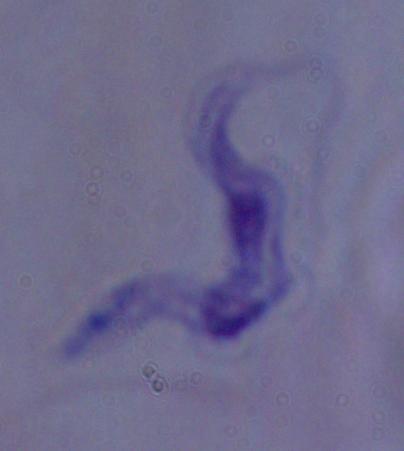

magnification = 1000x
identification = trypanosome
modality = photomicrograph